Name the parasite shown.
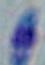

This is Toxoplasma gondii.

modality = photomicrograph
magnification = 1000x